Identify the parasite.
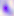
This is Toxoplasma gondii.

{
  "magnification": "400x",
  "modality": "micrograph"
}